State the blood parasite species.
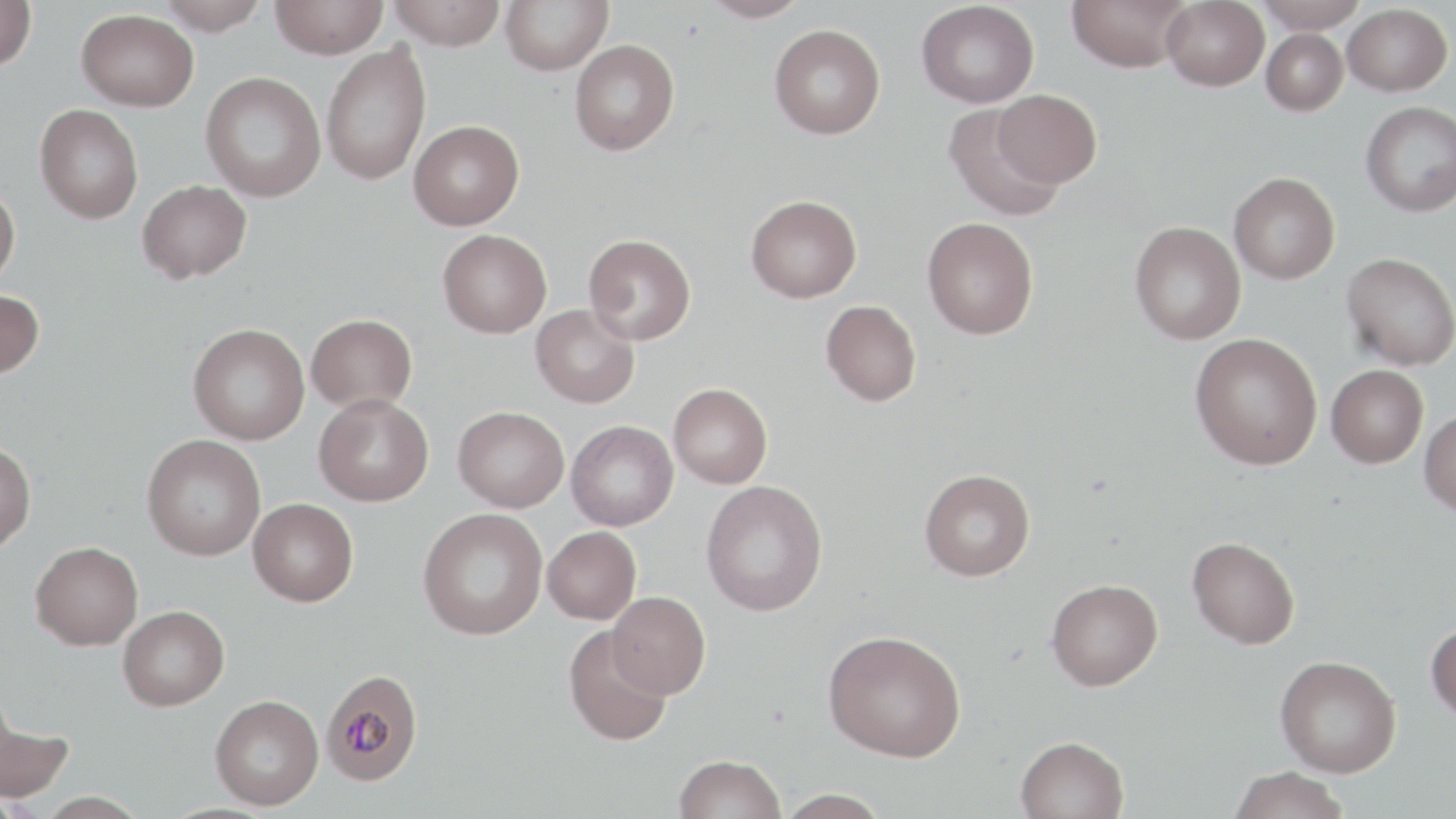
Plasmodium malariae.

modality = light microscopy
uninfected red blood cell locations = approximate bounding boxes as (x1, y1, x2, y2) in pixels: (0, 0, 37, 70), (158, 0, 268, 34), (387, 0, 506, 50), (500, 0, 613, 75), (699, 0, 811, 22), (1066, 0, 1193, 72), (1255, 0, 1365, 33), (270, 1, 388, 59), (916, 1, 1039, 108), (1161, 1, 1269, 90), (1343, 3, 1452, 96), (76, 8, 199, 111), (769, 24, 886, 139), (1262, 28, 1348, 115), (569, 39, 681, 155), (320, 43, 431, 185), (200, 71, 326, 202), (994, 90, 1102, 188), (1361, 101, 1456, 217), (34, 104, 144, 224), (942, 104, 1067, 222), (409, 120, 524, 230), (1229, 172, 1340, 284), (137, 179, 252, 283), (0, 181, 20, 289), (746, 195, 862, 302), (922, 217, 1039, 339), (1130, 221, 1245, 345), (438, 229, 552, 338), (584, 233, 696, 345), (1342, 252, 1456, 371), (0, 289, 45, 380), (821, 299, 921, 406), (530, 304, 639, 408), (306, 313, 417, 412), (188, 323, 309, 445), (1190, 333, 1323, 470), (1326, 365, 1428, 468), (669, 383, 772, 488), (313, 394, 434, 506), (453, 406, 568, 512), (1419, 409, 1456, 516), (567, 420, 678, 530), (142, 434, 266, 560), (0, 442, 36, 554), (919, 469, 1035, 581), (701, 480, 828, 616), (248, 498, 358, 606), (418, 507, 547, 640), (543, 526, 641, 624), (1187, 536, 1300, 649), (30, 541, 143, 650), (1046, 578, 1163, 690), (608, 591, 711, 698), (117, 605, 229, 711), (1426, 619, 1456, 723), (563, 626, 673, 747), (823, 630, 966, 762), (1275, 655, 1402, 777), (210, 694, 324, 809), (0, 704, 75, 804), (1015, 736, 1129, 819), (674, 754, 786, 819), (1228, 766, 1350, 819), (775, 788, 893, 818), (33, 791, 151, 819)
preparation = thin blood film
field of view = single
stain = May-Grünwald-Giemsa
magnification = 1000x
Plasmodium malariae-infected red blood cell locations = approximate bounding boxes as (x1, y1, x2, y2) in pixels: (320, 670, 424, 790)
image size = 1456×819 pixels